Outline each Plasmodium ovale-infected red blood cell.
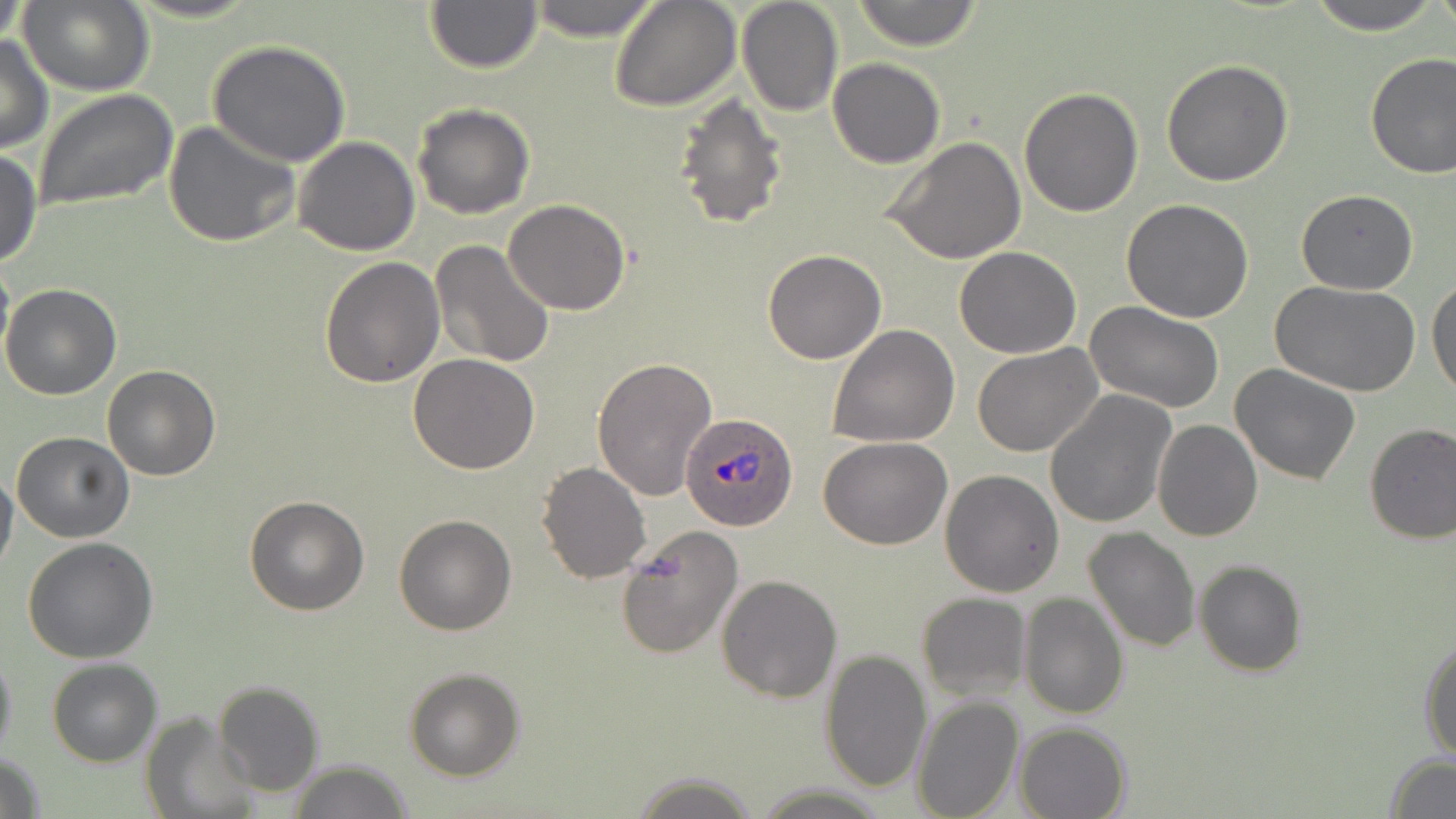

Approximate bounding boxes as (x1,y1)-(x2,y2) corner pairs in pixels.
Plasmodium ovale-infected red blood cells: (681,412)-(799,532).

Summary:
  - Uninfected red blood cell locations: (1,0)-(30,50), (20,0)-(154,95), (525,0)-(661,41), (610,0)-(741,111), (737,0)-(843,117), (852,0)-(984,51), (1308,0)-(1442,33), (425,3)-(542,73), (0,36)-(52,153), (207,41)-(351,167), (1364,52)-(1456,178), (827,58)-(944,167), (1161,60)-(1294,186), (1019,87)-(1143,217), (33,88)-(178,213), (672,92)-(791,231), (411,102)-(536,219), (163,120)-(299,248), (294,137)-(421,257), (883,137)-(1028,264), (0,149)-(43,269), (1295,189)-(1418,293), (1121,198)-(1254,321), (503,199)-(632,314), (429,240)-(556,368), (953,247)-(1082,358), (762,248)-(887,364), (0,255)-(13,375), (319,256)-(446,389), (1428,278)-(1456,400), (1270,280)-(1421,396), (1,284)-(122,401), (1084,302)-(1225,415), (828,324)-(960,448), (973,345)-(1102,458), (407,353)-(542,475), (591,355)-(718,503), (1230,363)-(1362,485), (102,364)-(220,480), (1045,391)-(1175,528), (1153,418)-(1263,540), (1363,423)-(1456,545), (11,430)-(135,543), (819,437)-(951,550), (536,462)-(653,585), (0,464)-(19,579), (939,469)-(1065,596), (245,495)-(368,615), (393,514)-(516,636), (614,524)-(746,660), (1081,526)-(1200,651), (24,537)-(158,663), (1194,560)-(1306,677), (716,574)-(841,703), (916,591)-(1030,701), (1019,592)-(1130,719), (1420,634)-(1456,762), (0,644)-(17,765), (819,648)-(933,793), (47,658)-(162,767), (405,668)-(525,780), (213,679)-(325,796), (911,697)-(1024,819), (143,711)-(259,818), (1014,721)-(1134,819), (0,751)-(46,818), (1384,753)-(1456,819), (287,760)-(416,818), (629,772)-(762,819), (751,783)-(893,816)
  - Slide-level diagnosis: Plasmodium ovale
  - Modality: optical microscopy
  - Preparation: thin blood film
  - Stain: May-Grünwald-Giemsa
  - Magnification: 1000x
  - Image size: 1456×819 pixels
  - Field of view: one of a larger specimen